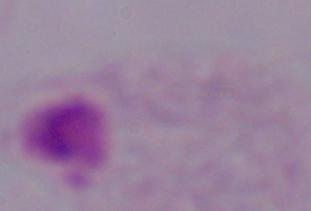
modality = micrograph
identification = trichomonad
magnification = 1000x